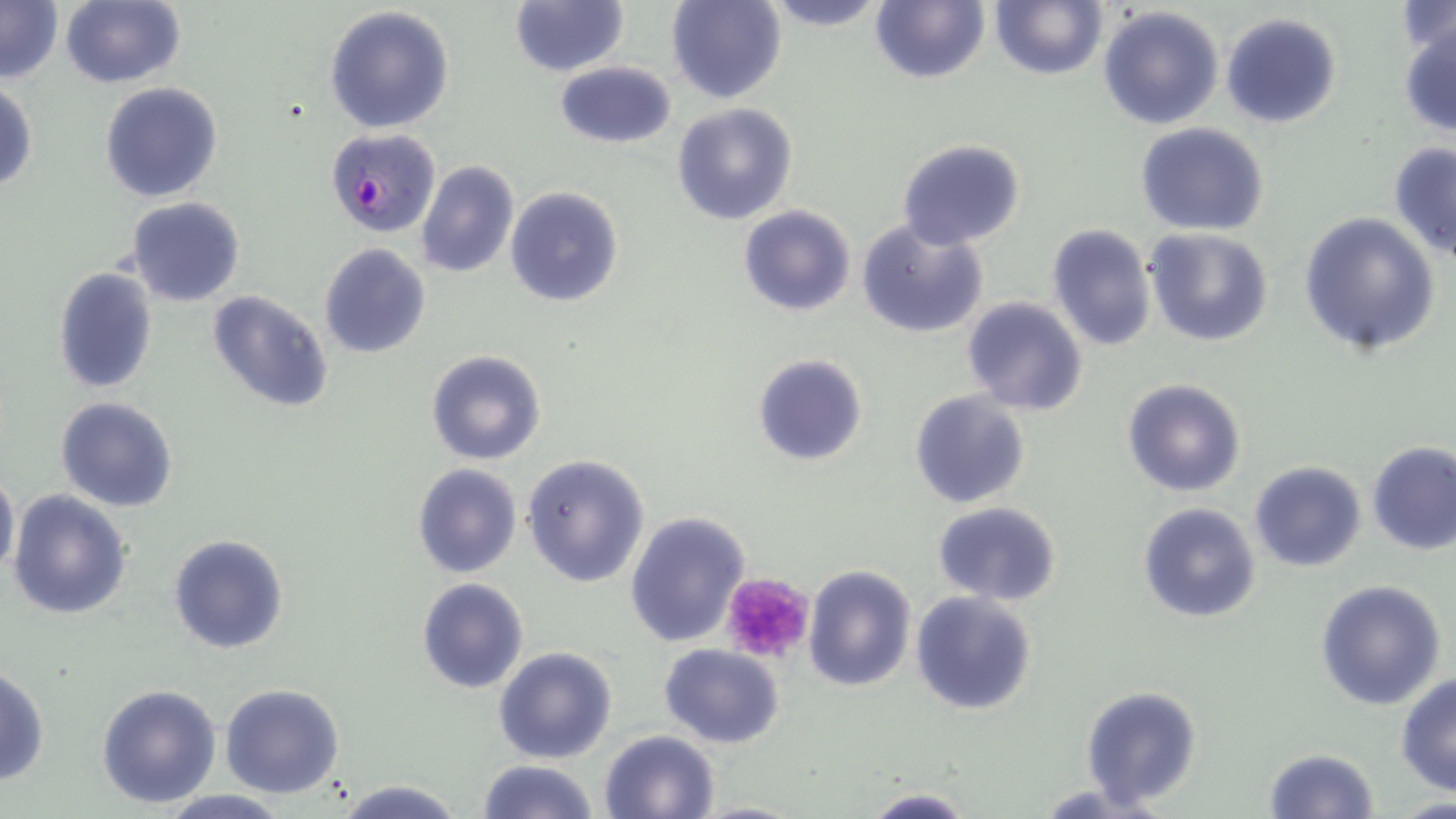
Plasmodium falciparum-infected red blood cell locations = approximate bounding boxes as named x1/y1/x2/y2 corners in pixels: (x1=327, y1=127, x2=442, y2=236)
slide-level diagnosis = Plasmodium falciparum
preparation = thin blood film
magnification = 1000x
uninfected red blood cell locations = approximate bounding boxes as named x1/y1/x2/y2 corners in pixels: (x1=0, y1=0, x2=62, y2=84), (x1=59, y1=0, x2=186, y2=89), (x1=665, y1=0, x2=786, y2=105), (x1=754, y1=0, x2=893, y2=30), (x1=869, y1=0, x2=989, y2=85), (x1=990, y1=0, x2=1106, y2=81), (x1=510, y1=2, x2=628, y2=76), (x1=1394, y1=3, x2=1455, y2=58), (x1=324, y1=5, x2=455, y2=134), (x1=1097, y1=6, x2=1226, y2=131), (x1=1220, y1=11, x2=1344, y2=129), (x1=1397, y1=22, x2=1456, y2=139), (x1=555, y1=60, x2=676, y2=150), (x1=1, y1=81, x2=37, y2=195), (x1=100, y1=81, x2=222, y2=203), (x1=671, y1=103, x2=798, y2=226), (x1=1136, y1=123, x2=1271, y2=236), (x1=896, y1=138, x2=1025, y2=250), (x1=1389, y1=142, x2=1456, y2=262), (x1=414, y1=161, x2=519, y2=279), (x1=505, y1=186, x2=624, y2=308), (x1=126, y1=198, x2=245, y2=308), (x1=738, y1=205, x2=855, y2=316), (x1=1298, y1=214, x2=1439, y2=356), (x1=855, y1=219, x2=988, y2=341), (x1=1047, y1=223, x2=1157, y2=352), (x1=1144, y1=228, x2=1274, y2=348), (x1=319, y1=243, x2=431, y2=360), (x1=52, y1=266, x2=159, y2=395), (x1=208, y1=291, x2=331, y2=415), (x1=961, y1=297, x2=1088, y2=418), (x1=425, y1=348, x2=547, y2=466), (x1=752, y1=353, x2=870, y2=467), (x1=1122, y1=378, x2=1248, y2=498), (x1=909, y1=390, x2=1032, y2=511), (x1=54, y1=396, x2=180, y2=512), (x1=1367, y1=441, x2=1456, y2=556), (x1=521, y1=454, x2=650, y2=587), (x1=1247, y1=460, x2=1367, y2=572), (x1=412, y1=464, x2=523, y2=580), (x1=0, y1=468, x2=19, y2=583), (x1=7, y1=487, x2=133, y2=620), (x1=931, y1=502, x2=1062, y2=604), (x1=1137, y1=502, x2=1262, y2=624), (x1=624, y1=511, x2=750, y2=648), (x1=167, y1=533, x2=291, y2=656), (x1=802, y1=563, x2=918, y2=693), (x1=416, y1=577, x2=529, y2=695), (x1=1314, y1=579, x2=1447, y2=711), (x1=910, y1=592, x2=1039, y2=717), (x1=658, y1=644, x2=784, y2=748), (x1=493, y1=646, x2=619, y2=765), (x1=0, y1=665, x2=50, y2=786), (x1=1395, y1=672, x2=1456, y2=795), (x1=95, y1=682, x2=222, y2=807), (x1=220, y1=684, x2=345, y2=800), (x1=1079, y1=684, x2=1203, y2=809), (x1=600, y1=730, x2=722, y2=819), (x1=1263, y1=747, x2=1380, y2=818), (x1=475, y1=759, x2=600, y2=818), (x1=333, y1=778, x2=467, y2=819), (x1=857, y1=787, x2=979, y2=819), (x1=155, y1=790, x2=296, y2=819), (x1=690, y1=800, x2=808, y2=818)
stain = May-Grünwald-Giemsa
field of view = single
platelet locations = approximate bounding boxes as named x1/y1/x2/y2 corners in pixels: (x1=720, y1=572, x2=815, y2=664)
modality = light microscopy
image size = 1456×819 pixels